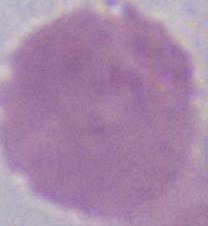 Captured at 1000x magnification. Micrograph. A red blood cell is shown.